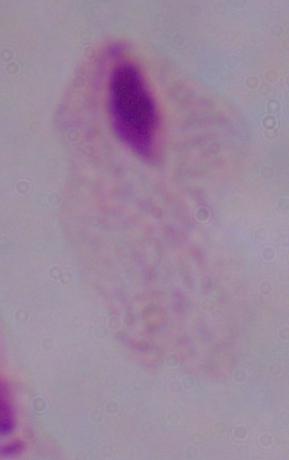
modality: photomicrograph
identification: trichomonad
magnification: 1000x